Locate every blood parasite and identify its species.
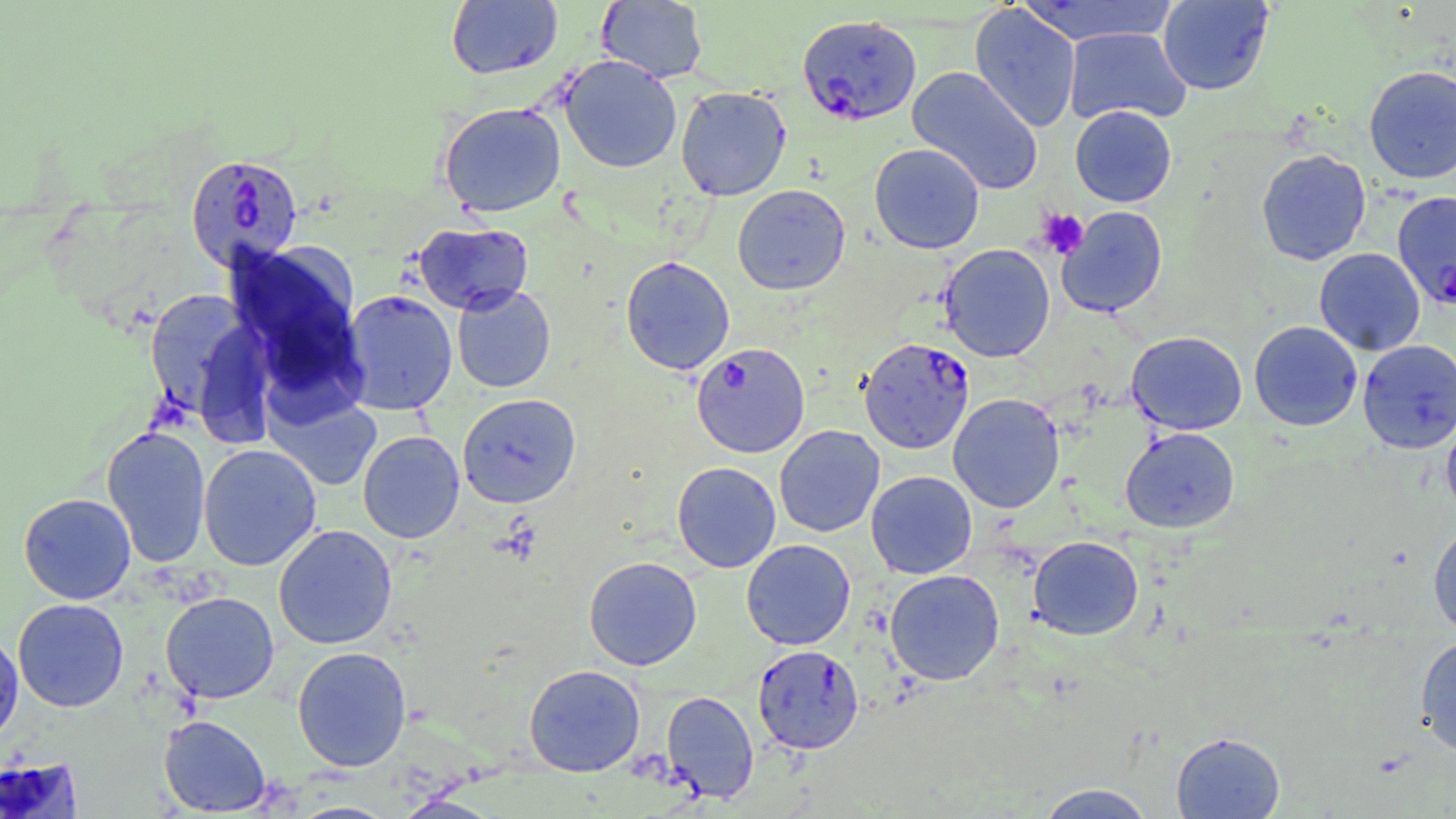
Approximate bounding boxes as (x1, y1, x2, y2) in pixels.
Plasmodium falciparum-infected red blood cells: (797, 14, 921, 126), (185, 153, 303, 271), (1394, 187, 1456, 308), (858, 337, 975, 454), (691, 341, 810, 458), (752, 644, 864, 754).
No Plasmodium ovale, Plasmodium malariae, Plasmodium vivax, Babesia divergens, or Trypanosoma brucei observed.

slide-level diagnosis = Plasmodium falciparum
field of view = one of a larger specimen
image size = 1456×819 pixels
platelet locations = approximate bounding boxes as (x1, y1, x2, y2) in pixels: (1036, 207, 1089, 259)
preparation = thin blood smear
stain = May-Grünwald-Giemsa
magnification = 1000x
modality = optical microscopy
uninfected red blood cell locations = approximate bounding boxes as (x1, y1, x2, y2) in pixels: (597, 0, 708, 83), (1157, 0, 1274, 95), (446, 1, 563, 79), (1019, 1, 1178, 45), (969, 3, 1081, 134), (1063, 27, 1191, 126), (559, 55, 683, 173), (1363, 65, 1456, 184), (907, 66, 1043, 195), (675, 85, 791, 201), (438, 102, 566, 217), (1070, 105, 1176, 207), (869, 143, 985, 254), (1256, 149, 1371, 265), (732, 184, 850, 295), (1056, 206, 1168, 317), (413, 221, 533, 314), (225, 242, 364, 401), (939, 243, 1055, 362), (1314, 248, 1425, 356), (620, 255, 735, 375), (452, 285, 556, 392), (143, 289, 265, 427), (340, 290, 458, 416), (1249, 321, 1363, 431), (1126, 331, 1247, 435), (1357, 339, 1456, 453), (265, 389, 382, 492), (458, 393, 581, 508), (948, 393, 1065, 513), (1441, 415, 1456, 521), (101, 425, 211, 568), (774, 425, 885, 537), (1120, 427, 1240, 533), (358, 430, 465, 543), (198, 443, 322, 571), (671, 462, 781, 572), (866, 471, 977, 579), (18, 493, 136, 604), (1428, 522, 1456, 637), (273, 524, 397, 649), (1028, 536, 1144, 640), (741, 539, 856, 650), (583, 556, 702, 670), (885, 569, 1004, 685), (160, 591, 279, 703), (12, 598, 129, 712), (0, 630, 24, 747), (1414, 636, 1456, 757), (292, 646, 411, 772), (524, 664, 645, 777), (661, 690, 759, 803), (158, 715, 271, 815), (1171, 731, 1285, 818), (0, 757, 83, 818), (1035, 783, 1157, 818)